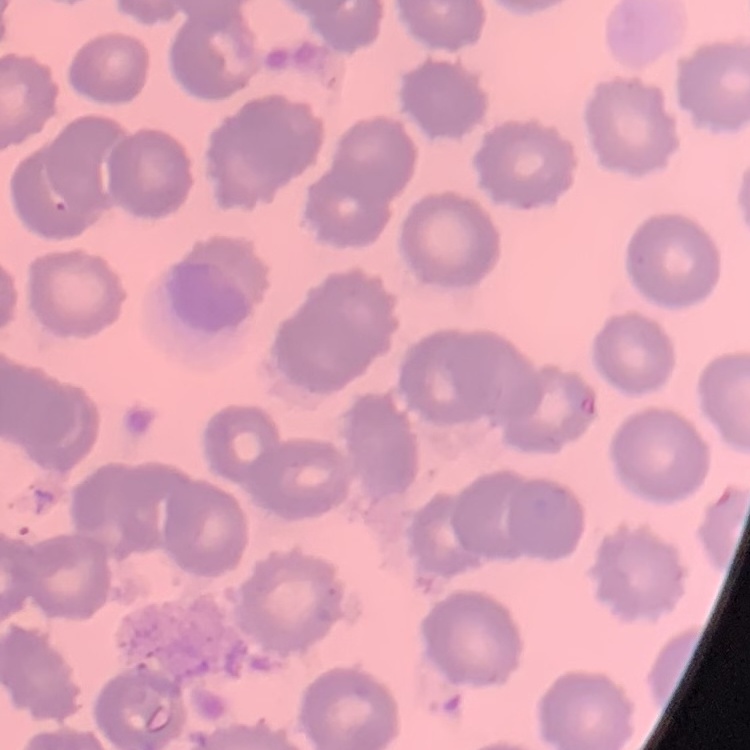 The red blood cells show no rouleaux formation. One tile cut from a larger photomicrograph. Field's or Giemsa stain. Thin blood smear.